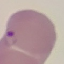

Summary:
  - Result: malaria parasites detected
  - Capture: smartphone through the microscope eyepiece
  - Image type: cell patch, automatically extracted from a larger field of view and resized to 64 × 64 pixels
  - Preparation: thin blood film
  - Stain: Giemsa